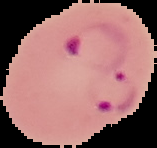
Summary:
  - Image type: cell region segmented out of the field of view; surrounding area masked to black
  - Malaria status: parasitized
  - Image size: 157×148 pixels
  - Preparation: thin blood smear